Identify the preparation type.
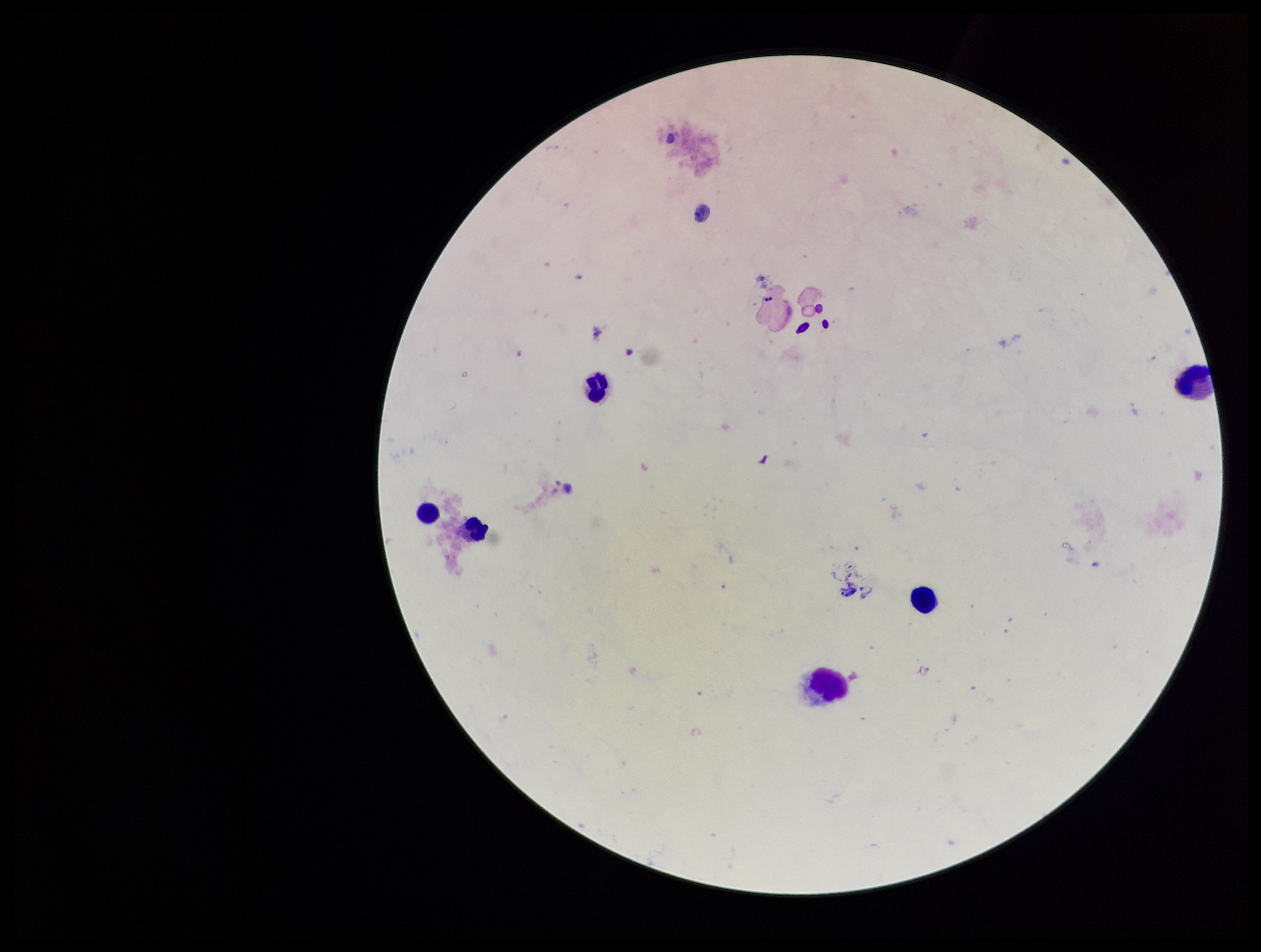

It is a thick blood smear.

Patient malaria status: negative. Parasite count: 0. Giemsa stain. Plasmodium parasites: none seen. One field from this slide. Leukocyte count: 6. Photographed through the microscope eyepiece with a smartphone camera. Image is 1261×952 pixels.